Report the malaria status of this cell.
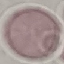
It is uninfected.

Summary:
  - Stain: Giemsa
  - Capture: smartphone camera at the microscope eyepiece
  - Preparation: thin blood film
  - Image type: cell patch, automatically extracted from a larger field of view and resized to 64 × 64 pixels